Point out each leukocyte.
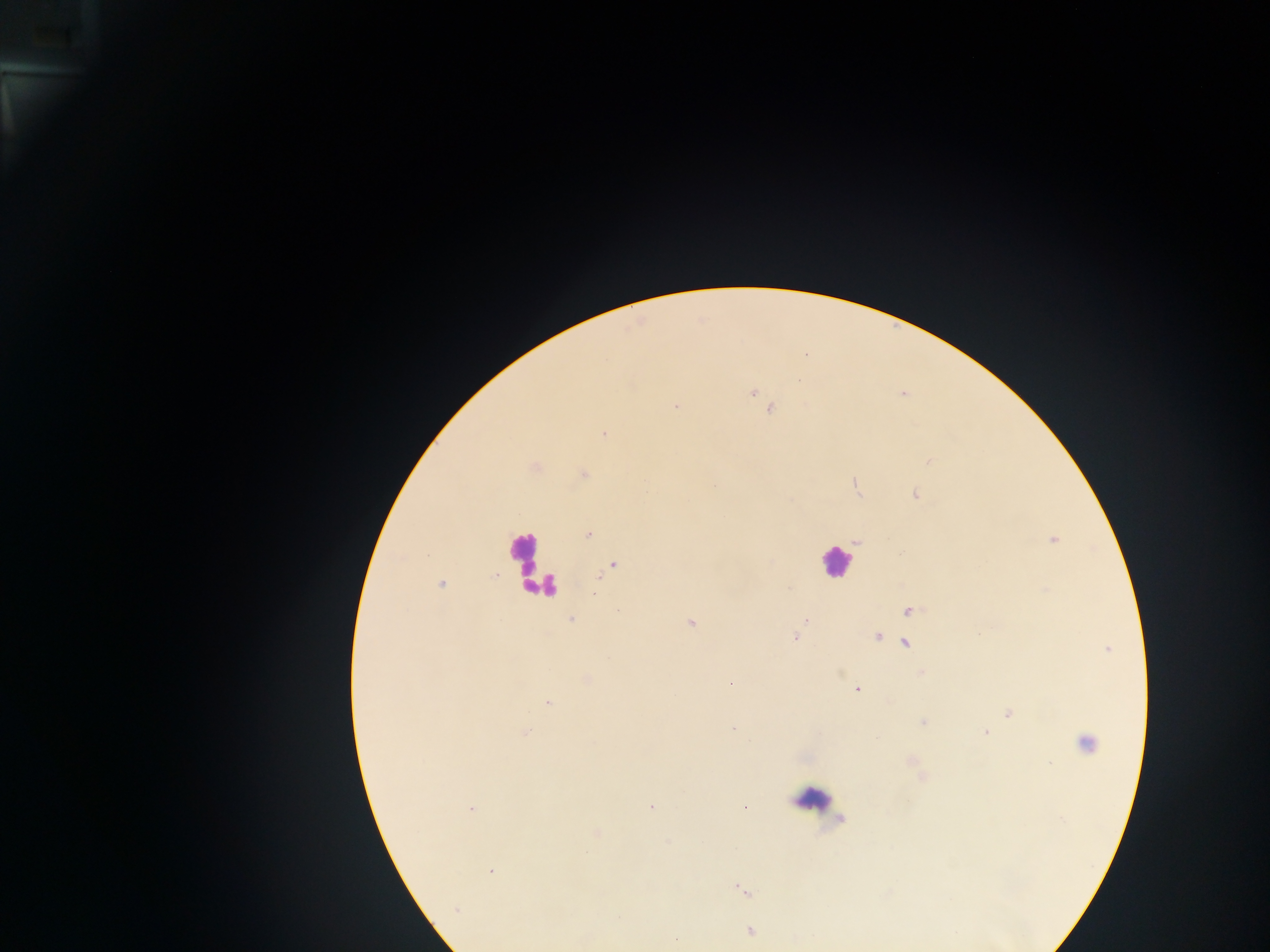
Approximate centers as x y in pixels.
Leukocytes: 524 556; 835 562; 816 798.

field of view = single
Plasmodium parasite locations = approximate centers as x y in pixels: 753 392; 903 395; 676 405; 770 410; 604 434; 929 462; 535 467; 584 475; 856 487; 915 495; 587 534; 1053 540; 856 542; 611 566; 442 584; 594 593; 618 610; 910 611; 570 619; 805 620; 691 622; 877 636; 794 637; 904 644; 730 683; 856 689; 547 703; 1009 714; 922 722; 733 729; 526 732; 985 732; 1086 741; 651 807; 471 809; 596 833; 490 871; 741 889; 456 909; 750 931; 677 938
country = Ghana
capture = mobile-phone photograph through a microscope
image size = 1270×952 pixels
preparation = thick blood smear